Outline each blood parasite and name the species.
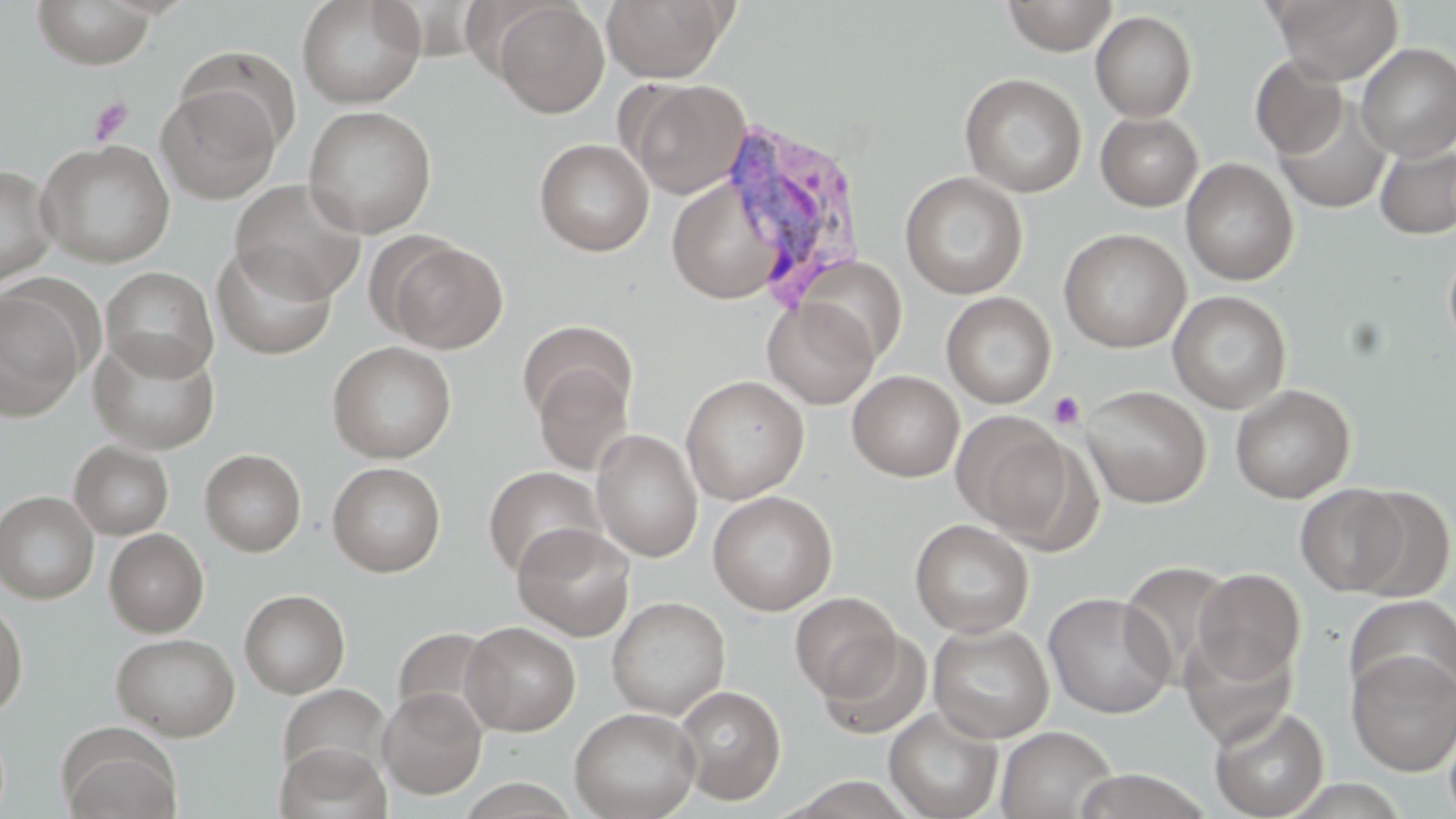

Approximate bounding boxes as (x1, y1, x2, y2) in pixels.
Plasmodium vivax-infected red blood cells: (715, 118, 870, 309).
No Plasmodium falciparum, Plasmodium ovale, Plasmodium malariae, Babesia divergens, or Trypanosoma brucei observed.

Summary:
  - Uninfected red blood cell locations: (296, 0, 426, 108), (601, 0, 731, 83), (1001, 0, 1118, 55), (1271, 0, 1403, 84), (31, 1, 159, 69), (492, 1, 609, 118), (1091, 10, 1197, 122), (1356, 43, 1456, 161), (1250, 54, 1349, 160), (959, 73, 1086, 197), (623, 77, 752, 199), (157, 83, 282, 204), (1273, 95, 1392, 214), (303, 105, 437, 238), (1096, 112, 1204, 211), (534, 138, 654, 256), (37, 139, 175, 268), (1374, 141, 1456, 240), (1181, 158, 1299, 286), (0, 165, 57, 286), (900, 171, 1028, 299), (666, 177, 788, 304), (230, 179, 367, 304), (1058, 228, 1191, 352), (382, 239, 507, 353), (1443, 242, 1456, 357), (212, 243, 337, 360), (793, 255, 908, 365), (101, 266, 219, 381), (1, 288, 88, 423), (1168, 290, 1292, 413), (941, 291, 1056, 409), (762, 296, 880, 409), (517, 320, 636, 427), (90, 334, 220, 454), (327, 341, 457, 463), (531, 361, 634, 476), (847, 371, 964, 482), (681, 374, 810, 505), (1230, 384, 1355, 504), (1080, 385, 1211, 507), (952, 411, 1079, 539), (591, 429, 703, 563), (69, 441, 174, 539), (200, 449, 307, 556), (327, 461, 446, 577), (483, 465, 606, 580), (1295, 483, 1411, 596), (1347, 486, 1454, 601), (0, 490, 99, 604), (707, 490, 838, 616), (909, 518, 1034, 638), (512, 523, 636, 642), (104, 529, 209, 637), (1117, 559, 1238, 686), (1192, 568, 1306, 685), (239, 589, 350, 698), (789, 591, 903, 702), (1042, 592, 1177, 718), (1345, 593, 1456, 703), (606, 597, 730, 719), (0, 598, 28, 718), (461, 622, 581, 735), (927, 622, 1054, 743), (391, 626, 504, 733), (818, 630, 933, 739), (1178, 630, 1299, 748), (111, 632, 240, 741), (1347, 649, 1456, 776), (277, 683, 392, 787), (673, 684, 787, 805), (378, 687, 487, 799), (1209, 703, 1330, 819), (883, 706, 1004, 819), (569, 707, 701, 819), (1443, 717, 1456, 819), (56, 725, 182, 819), (996, 725, 1117, 818), (276, 742, 393, 819), (787, 776, 917, 818)
  - Platelet locations: (87, 96, 133, 146), (1047, 390, 1087, 430)
  - Slide-level diagnosis: Plasmodium vivax
  - Preparation: thin blood smear
  - Modality: light microscopy
  - Magnification: 1000x
  - Image size: 1456×819 pixels
  - Stain: May-Grünwald-Giemsa
  - Field of view: one of a larger specimen